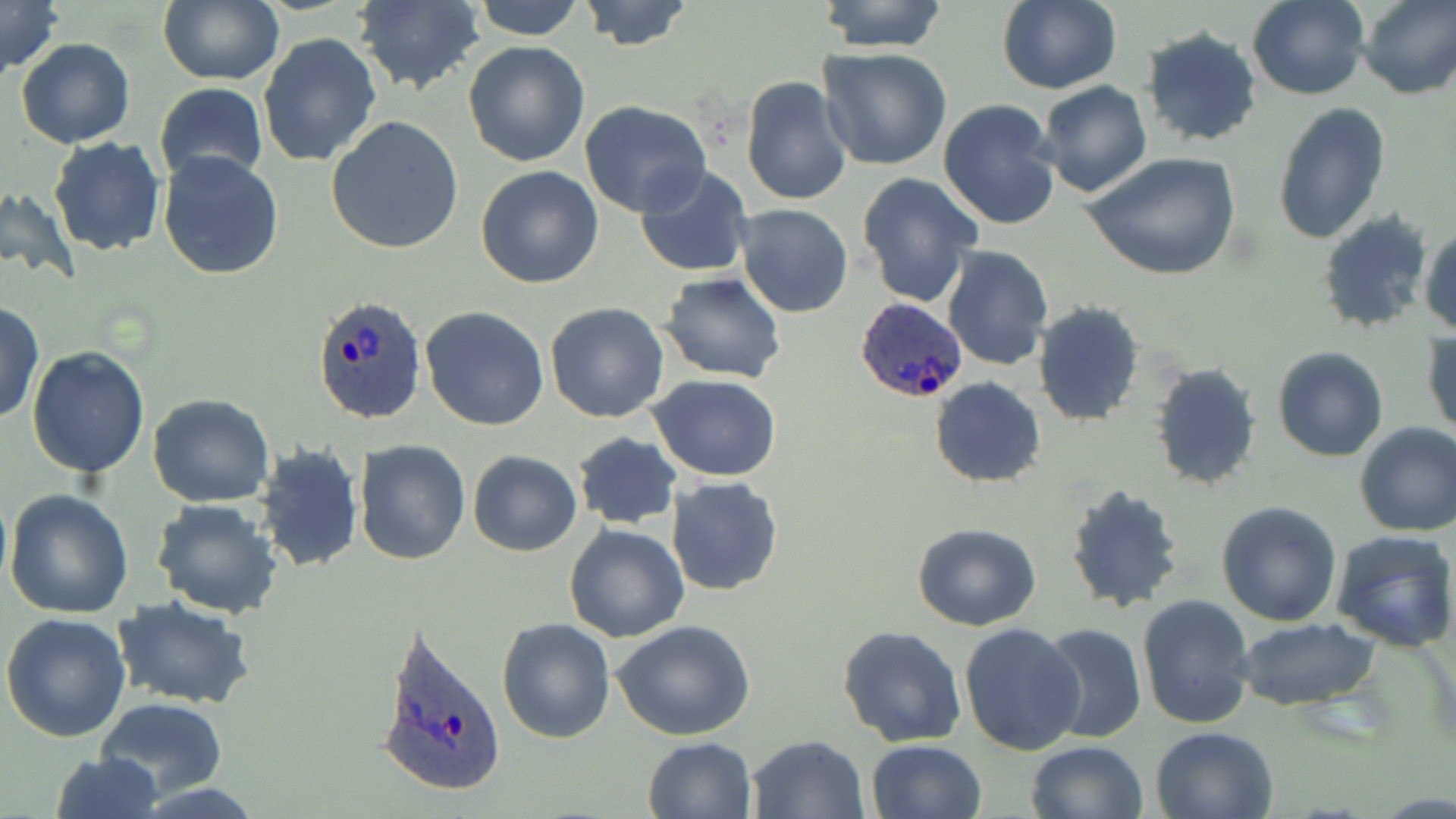 Approximate bounding boxes as [x1, y1, x2, y2] in pixels. Uninfected red blood cell locations: [157, 0, 284, 88], [352, 0, 485, 96], [471, 0, 585, 41], [575, 0, 695, 50], [816, 0, 950, 52], [1247, 0, 1369, 100], [1357, 0, 1455, 100], [0, 1, 63, 80], [998, 1, 1122, 95], [1140, 25, 1263, 148], [258, 35, 383, 170], [17, 38, 135, 149], [463, 40, 591, 168], [817, 46, 953, 171], [739, 76, 852, 208], [1036, 80, 1152, 198], [155, 83, 268, 184], [938, 98, 1062, 232], [579, 101, 712, 219], [1272, 104, 1390, 245], [325, 115, 464, 255], [48, 136, 165, 256], [158, 150, 286, 280], [1082, 152, 1244, 283], [633, 164, 756, 279], [475, 165, 604, 288], [856, 172, 983, 306], [1, 184, 82, 288], [735, 203, 853, 317], [1316, 212, 1436, 336], [1420, 222, 1456, 338], [941, 244, 1053, 370], [659, 272, 785, 383], [544, 301, 669, 423], [1031, 301, 1145, 426], [0, 302, 45, 428], [421, 307, 549, 430], [1422, 328, 1455, 440], [28, 346, 149, 478], [1272, 346, 1390, 462], [1148, 362, 1262, 492], [647, 374, 781, 483], [930, 376, 1046, 488], [148, 394, 276, 508], [1354, 422, 1456, 537], [571, 433, 683, 529], [354, 440, 470, 566], [253, 443, 365, 574], [466, 451, 582, 556], [664, 476, 783, 597], [1063, 483, 1187, 614], [4, 488, 133, 619], [152, 499, 283, 619], [1216, 501, 1343, 625], [564, 524, 689, 642], [912, 524, 1042, 631], [1331, 528, 1456, 655], [1136, 593, 1256, 729], [115, 597, 258, 711], [1, 612, 131, 741], [497, 617, 615, 741], [611, 619, 755, 740], [1233, 619, 1381, 711], [959, 622, 1087, 757], [1036, 622, 1147, 745], [838, 627, 967, 747], [96, 697, 227, 801], [1150, 725, 1279, 819], [748, 735, 872, 819], [643, 736, 757, 819], [866, 739, 986, 819], [1023, 740, 1149, 819], [46, 751, 165, 819]. Plasmodium ovale-infected red blood cell locations: [311, 294, 427, 427], [853, 297, 970, 406], [374, 620, 508, 802]. Slide-level diagnosis: Plasmodium ovale. May-Grünwald-Giemsa-stained preparation. One field of a larger specimen. Light microscopy. Captured at 1000x magnification. Thin blood film. Image is 1456×819 pixels.